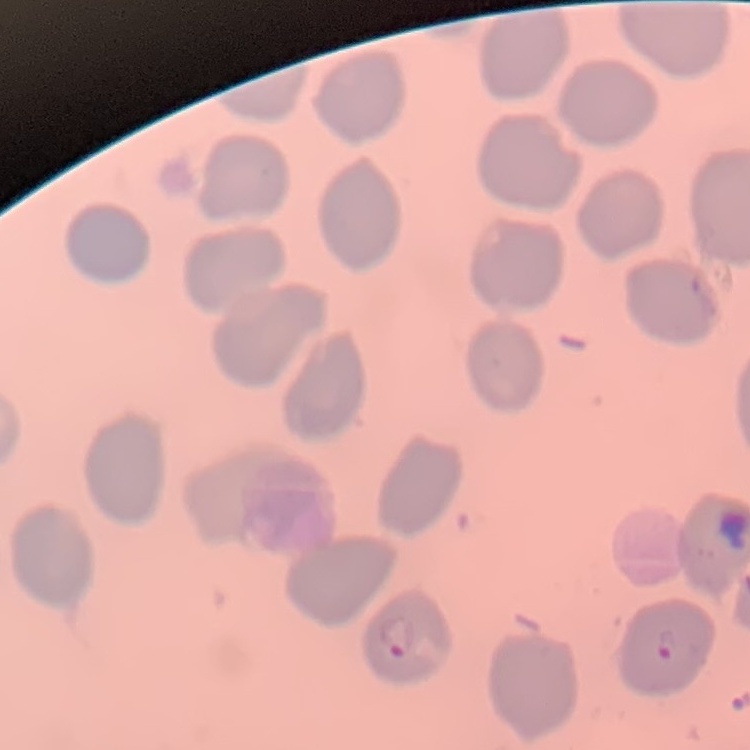

The red blood cells exhibit no rouleaux formation. Stained with either Field's or Giemsa. Thin blood smear. Square crop of a larger photomicrograph.